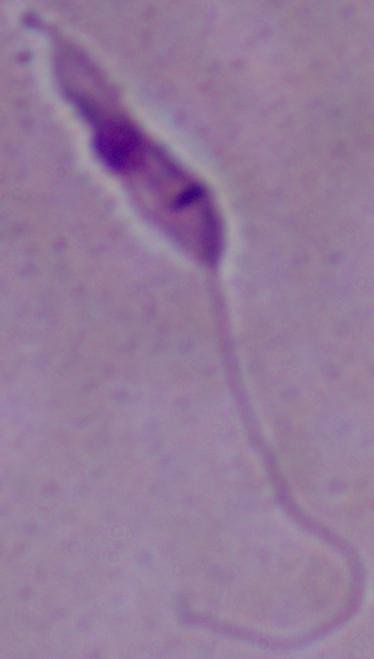
A Leishmania parasite is shown. Micrograph. Captured at 1000x magnification.